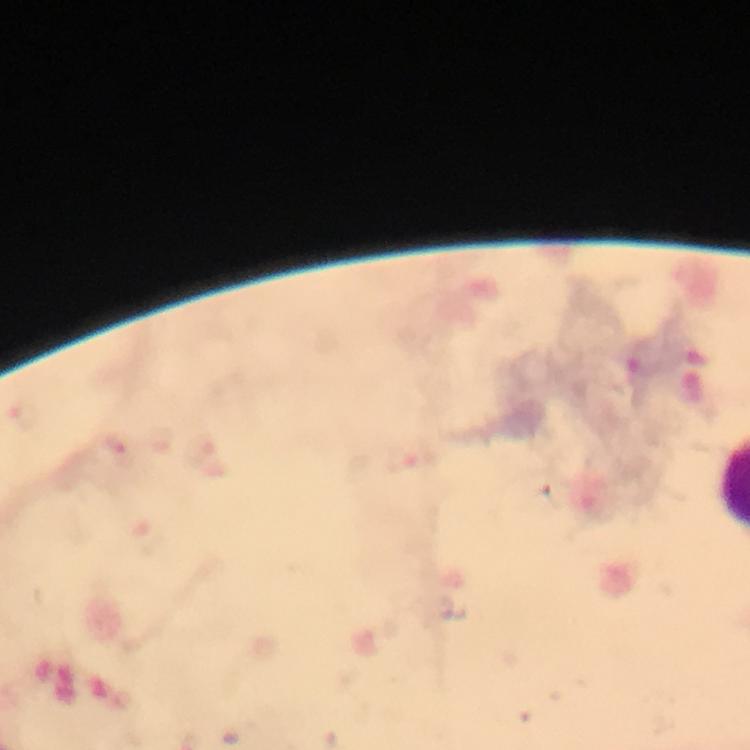
Approximate centers as [x, y] in pixels. Plasmodium parasite locations: [118, 444]. Immersion oil applied. Thick blood smear. At 100x magnification. Photographed with a smartphone mounted on the microscope. Giemsa stain. Cropped region of a single field of view. Image is 750×750 pixels. From a diagnostic examination for malaria.